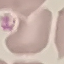 Malaria status: uninfected. Photographed with a smartphone camera at the microscope eyepiece. Giemsa-stained preparation. Cell patch, automatically extracted from a larger field of view and resized to 64 × 64 pixels. Thin blood smear.